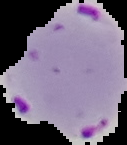

Summary:
  - Image size: 127×145 pixels
  - Preparation: thin blood smear
  - Image type: segmented cell region on a black background
  - Malaria status: parasitized